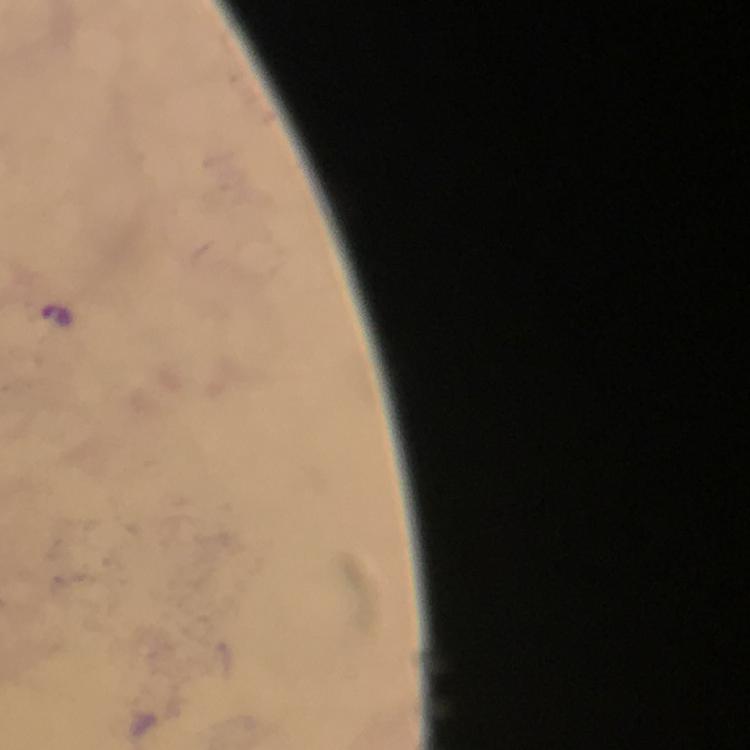
context = from a diagnostic examination for malaria
preparation = thick blood smear
malaria parasite locations = approximate centers as [x, y] in pixels: [56, 314]
stain = Giemsa
cropped from = one field of view
magnification = 100x
capture = smartphone mounted on the microscope
immersion oil = applied
image size = 750×750 pixels